Locate every leukocyte (white blood cell).
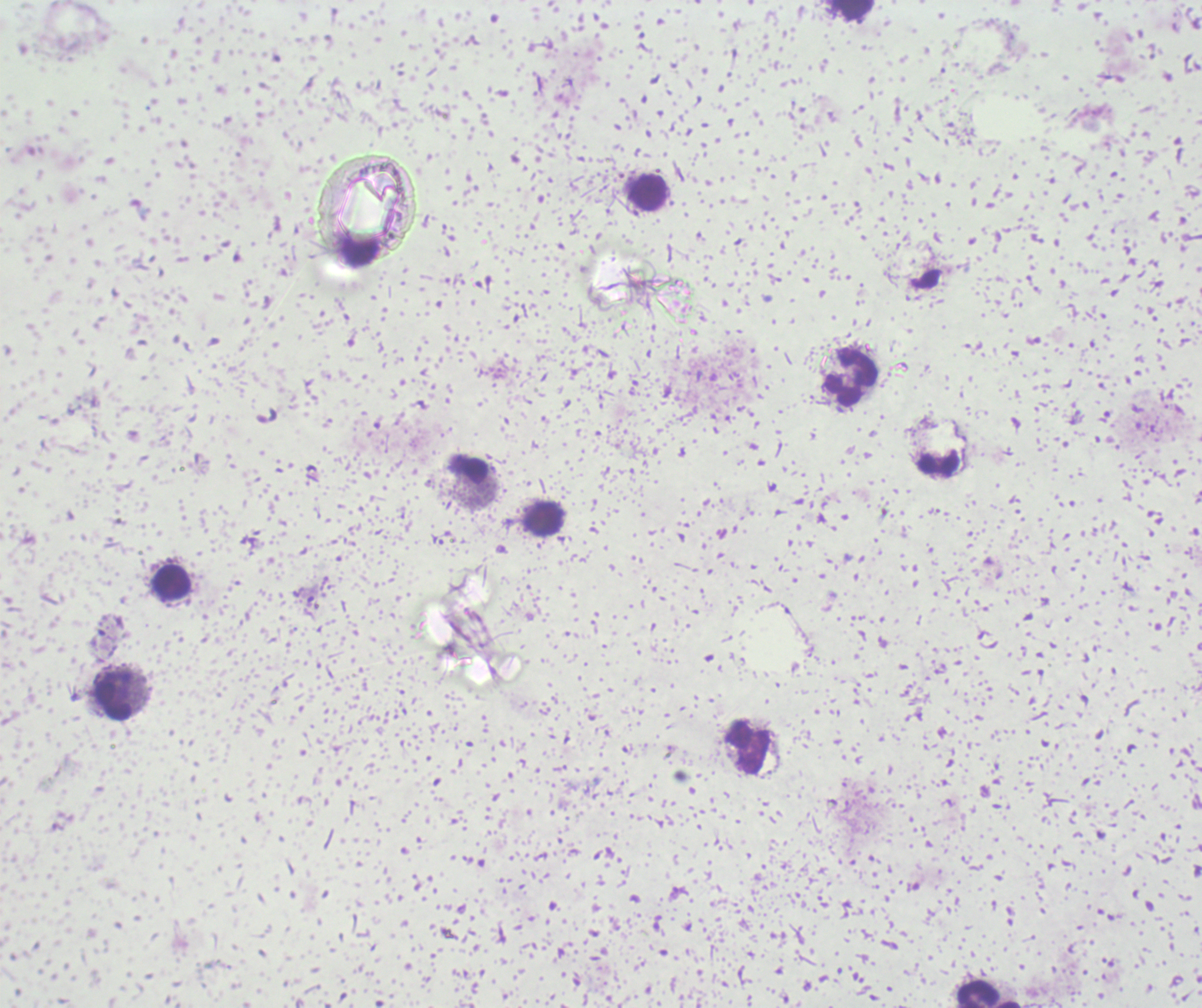
Approximate object centers, in pixels from the top-left corner.
Leukocytes: (x=850, y=9), (x=649, y=192), (x=851, y=379), (x=467, y=468), (x=544, y=517), (x=172, y=582), (x=115, y=692), (x=748, y=748), (x=976, y=993).

Previously used in an actual diagnosis. Single field of view. Thick blood film. Image is 1202×1008 pixels. Romanowsky stain. Captured at 100x magnification. Background quality: unsatisfactory. Result: no malaria parasites seen.